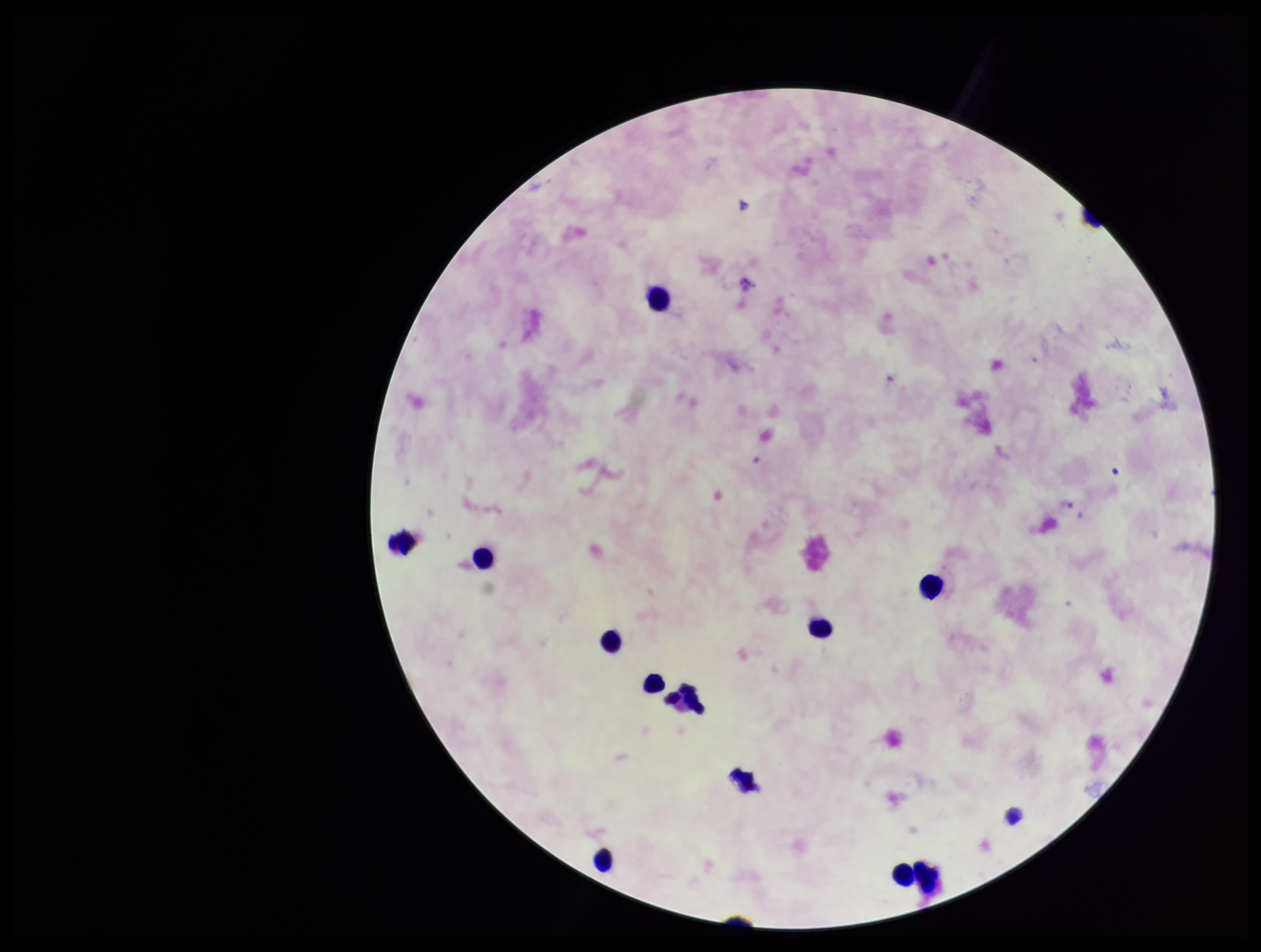
image size = 1261×952 pixels
patient malaria status = negative
leukocyte count = 12
parasite count = 0
Plasmodium parasites = none seen
stain = Giemsa
field of view = single
preparation = thick smear
capture = smartphone photograph through the microscope eyepiece